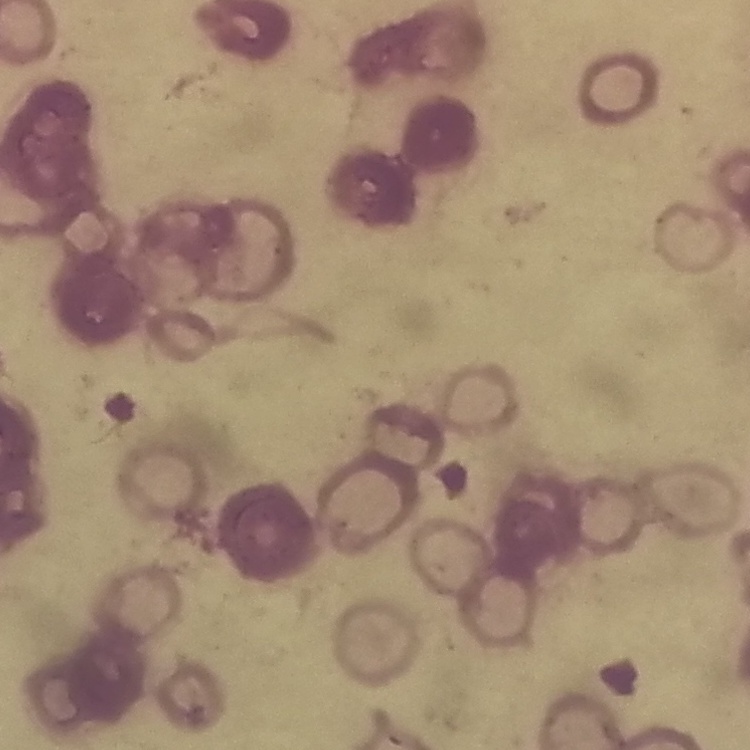
Summary:
  - Red blood cell morphology: rouleaux formation
  - Stain: Field's or Giemsa
  - Preparation: thin blood smear
  - Image type: one tile cut from a larger photomicrograph